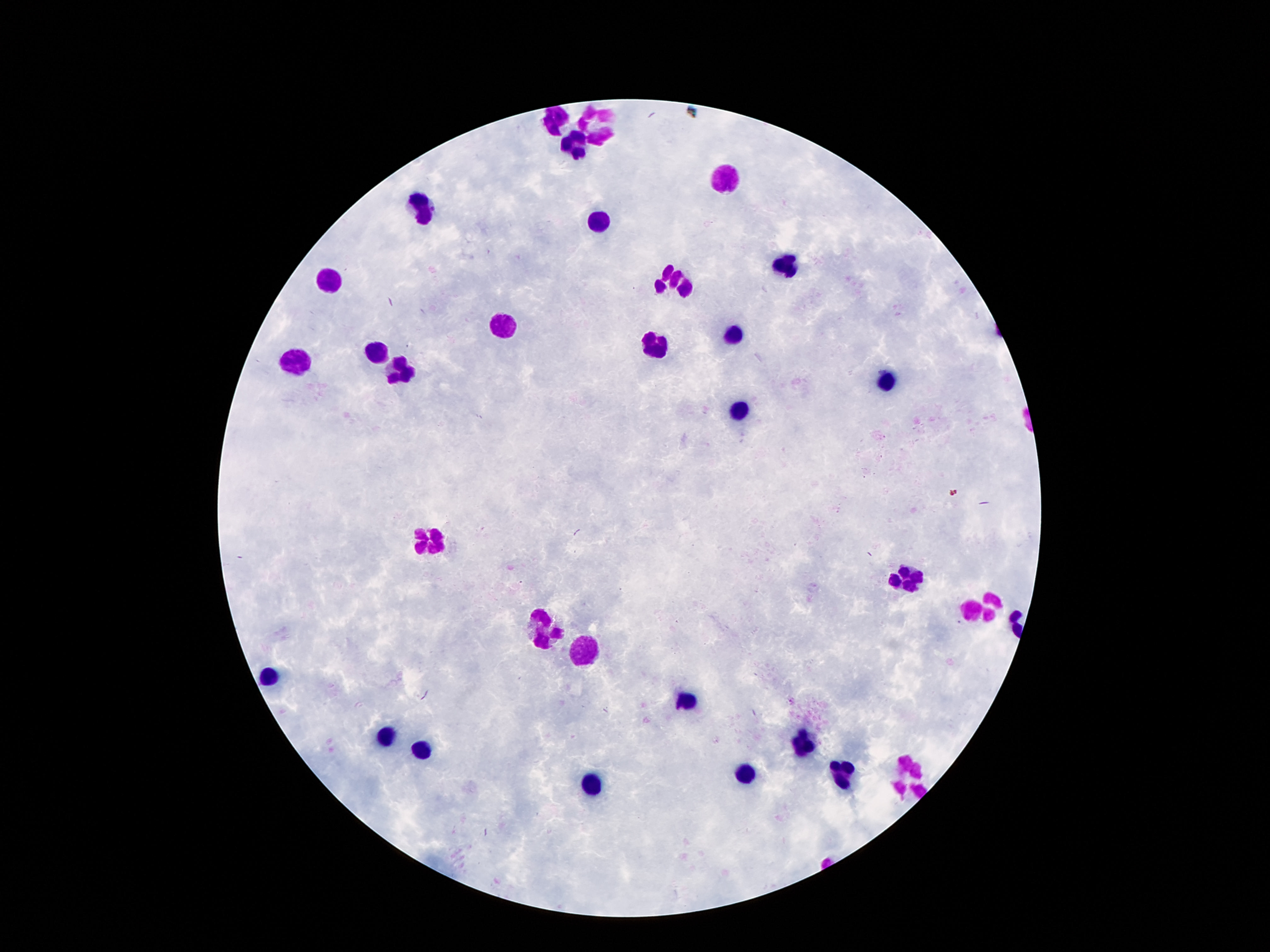 Approximate centers as [x, y] in pixels. Leukocyte locations: [561, 119], [597, 127], [575, 148], [725, 179], [424, 210], [599, 221], [787, 264], [672, 281], [329, 282], [500, 327], [734, 334], [659, 345], [376, 348], [294, 362], [400, 373], [886, 380], [741, 415], [427, 539], [906, 578], [981, 607], [544, 627], [586, 643], [272, 678], [685, 703], [385, 737], [802, 746], [422, 751], [747, 775], [842, 775], [909, 775], [590, 787]. 100x magnification. Giemsa stain. Thick blood film. Smartphone photograph taken through the microscope eyepiece. Patient malaria status: negative. Image is 1270×952 pixels. Single field of view.